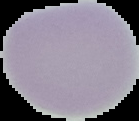

Summary:
  - Image type: segmented cell region on a black background
  - Malaria status: uninfected
  - Preparation: thin blood smear
  - Image size: 139×121 pixels